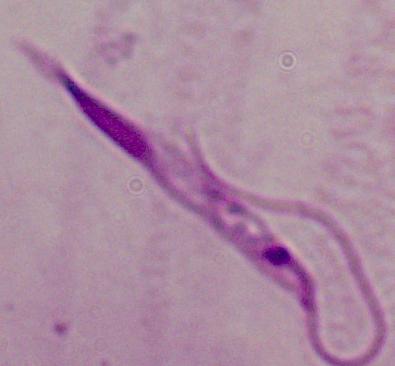
identification = Leishmania
magnification = 1000x
modality = photomicrograph